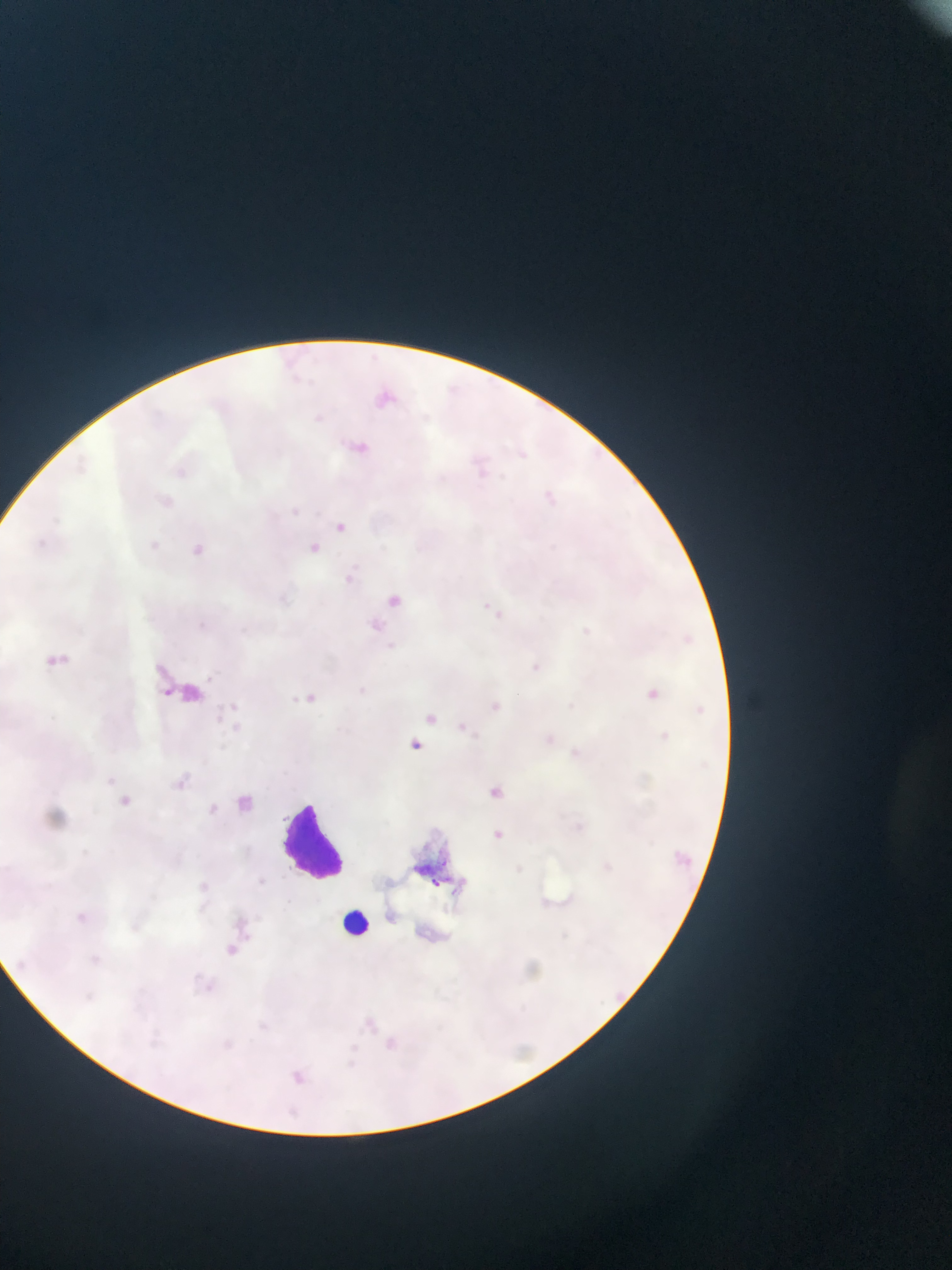
field of view = single
Plasmodium parasite locations = approximate bounding boxes as [left, top, right, bottom] in pixels: [361, 347, 385, 364], [284, 349, 301, 369], [286, 370, 312, 388], [448, 374, 484, 411], [369, 382, 397, 411], [312, 411, 328, 429], [353, 437, 375, 462], [513, 442, 536, 462], [474, 456, 503, 484], [540, 479, 567, 507], [154, 488, 174, 505], [284, 499, 307, 518], [47, 512, 64, 533], [333, 517, 349, 539], [28, 533, 60, 560], [152, 535, 167, 552], [303, 540, 320, 560], [193, 544, 205, 555], [347, 561, 363, 574], [338, 574, 362, 590], [387, 586, 412, 612], [490, 607, 511, 626], [192, 610, 230, 634], [372, 616, 392, 641], [571, 620, 592, 641], [679, 626, 696, 653], [44, 646, 77, 670], [525, 654, 548, 673], [205, 667, 224, 683], [288, 684, 311, 714], [647, 688, 659, 699], [223, 692, 243, 708], [486, 698, 507, 724], [693, 700, 710, 723], [422, 707, 437, 725], [229, 712, 259, 744], [211, 714, 229, 738], [462, 721, 472, 735], [649, 725, 677, 749], [534, 728, 565, 751], [407, 735, 424, 755], [100, 769, 116, 788], [173, 771, 199, 793], [483, 780, 498, 795], [233, 787, 267, 819], [116, 791, 141, 809], [205, 793, 221, 817], [496, 823, 508, 847], [675, 852, 712, 876], [598, 854, 613, 872], [253, 863, 276, 889], [191, 877, 228, 905], [64, 900, 101, 928], [240, 907, 261, 931], [222, 934, 242, 960], [87, 951, 114, 968], [13, 954, 30, 974], [200, 970, 227, 997], [76, 985, 111, 1020], [610, 987, 627, 1004], [356, 1009, 380, 1039], [256, 1013, 276, 1036], [147, 1023, 167, 1048], [382, 1029, 398, 1054], [221, 1033, 238, 1053], [337, 1044, 363, 1073], [285, 1050, 316, 1086], [279, 1098, 305, 1119]
leukocyte locations = approximate bounding boxes as [left, top, right, bottom] in pixels: [276, 796, 351, 882], [334, 905, 379, 945]
preparation = thin blood smear
country = Ghana
image size = 952×1270 pixels
capture = mobile-phone photograph through a microscope